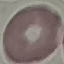 Result: no malaria parasites detected. Automatically extracted cell patch, resized to 64 × 64 pixels. Thin blood smear. Acquired by smartphone through the microscope eyepiece. Giemsa stain.